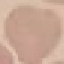

malaria status = uninfected
capture = smartphone camera at the microscope eyepiece
preparation = thin blood smear
image type = automatically extracted cell patch, resized to 64 × 64 pixels
stain = Giemsa